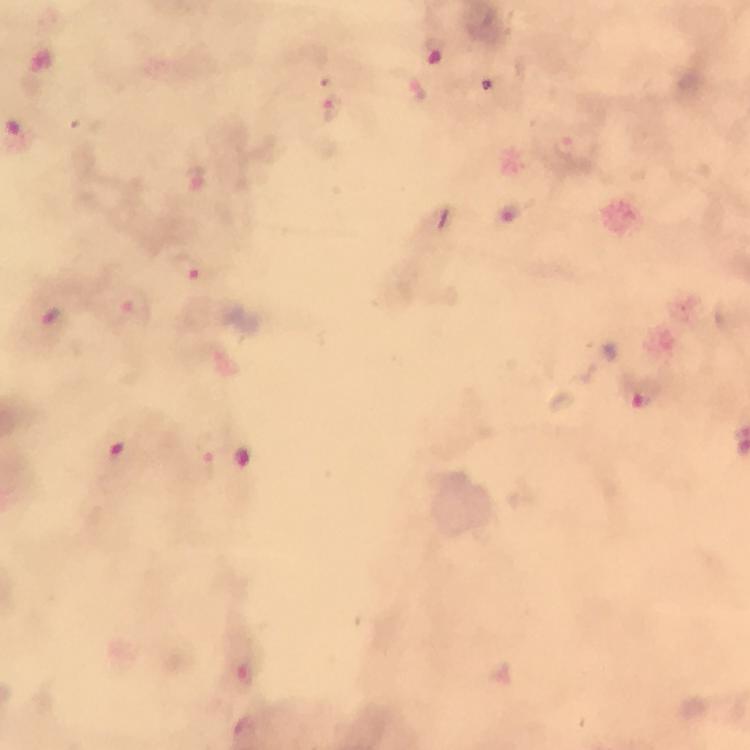
stain = Giemsa
context = from a malaria diagnostic workup
immersion oil = used
preparation = thick blood smear
capture = smartphone photograph through a microscope
cropped from = a single field of view
magnification = 100x
image size = 750×750 pixels
Plasmodium parasite locations = approximate centers as [x, y] in pixels: [437, 53], [333, 111], [565, 144], [199, 180], [187, 267], [137, 309], [644, 395], [120, 456], [243, 459], [245, 675]